Classify this cell by malaria status.
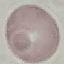
It is uninfected.

stain = Giemsa
capture = smartphone camera at the microscope eyepiece
preparation = thin blood film
image type = automatically extracted cell patch, resized to 64 × 64 pixels